Give the extent of all Plasmodium ovale-infected red blood cells.
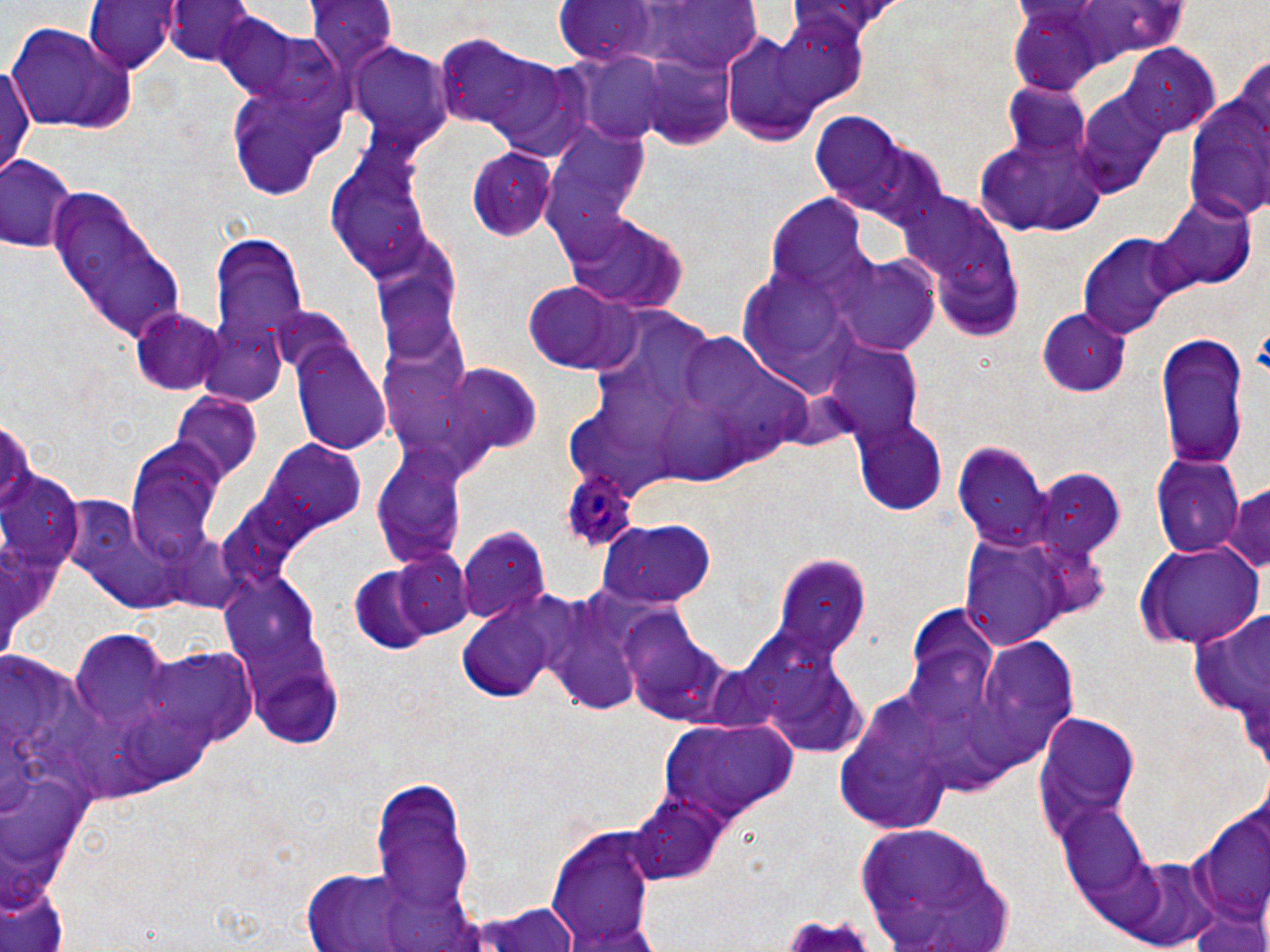
Approximate bounding boxes as [x1, y1, x2, y2] in pixels.
Plasmodium ovale-infected red blood cells: [563, 469, 640, 549].

Uninfected red blood cell locations: [84, 0, 180, 73], [166, 1, 257, 70], [304, 1, 400, 76], [771, 13, 869, 110], [213, 14, 337, 112], [3, 22, 136, 134], [716, 30, 836, 146], [432, 37, 552, 136], [346, 43, 453, 149], [1122, 48, 1218, 136], [572, 53, 677, 147], [640, 56, 741, 149], [486, 57, 597, 159], [0, 59, 36, 181], [221, 73, 348, 203], [1003, 84, 1093, 157], [1074, 89, 1169, 197], [1185, 95, 1269, 225], [807, 109, 943, 225], [971, 123, 1105, 238], [544, 131, 651, 243], [328, 139, 435, 281], [467, 146, 559, 240], [0, 154, 79, 256], [47, 183, 189, 343], [897, 193, 1020, 327], [769, 197, 868, 292], [1151, 199, 1254, 296], [563, 214, 687, 312], [207, 232, 308, 363], [371, 232, 469, 359], [1079, 235, 1186, 336], [834, 255, 940, 354], [522, 279, 636, 374], [268, 306, 356, 382], [131, 307, 225, 394], [1038, 308, 1132, 396], [196, 324, 289, 408], [683, 330, 774, 417], [1153, 334, 1251, 467], [290, 341, 392, 453], [829, 346, 925, 441], [419, 362, 543, 462], [581, 375, 692, 450], [170, 394, 263, 484], [663, 401, 741, 487], [852, 417, 948, 516], [120, 433, 230, 566], [955, 442, 1056, 550], [267, 443, 367, 532], [370, 444, 468, 564], [1153, 455, 1245, 557], [1032, 472, 1126, 561], [1223, 484, 1270, 579], [593, 519, 718, 605], [456, 526, 550, 625], [953, 528, 1096, 650], [1139, 545, 1265, 646], [392, 550, 475, 640], [770, 554, 872, 663], [350, 568, 435, 656], [222, 573, 326, 678], [541, 587, 667, 715], [452, 589, 578, 703], [1184, 600, 1270, 741], [901, 603, 998, 717], [618, 610, 745, 729], [68, 627, 182, 722], [973, 636, 1081, 761], [135, 646, 258, 749], [832, 691, 961, 833], [1030, 709, 1141, 848], [653, 715, 798, 825], [368, 774, 477, 912], [628, 795, 726, 886], [1196, 803, 1270, 930], [1058, 805, 1152, 900], [541, 820, 661, 952], [857, 821, 1012, 951], [1117, 856, 1221, 950], [294, 864, 482, 952], [0, 884, 67, 952], [460, 899, 583, 952], [1186, 904, 1269, 952]. Slide-level diagnosis: Plasmodium ovale. One field of a larger specimen. Thin blood film. Captured at 1000x magnification. Optical microscopy. Image is 1270×952 pixels. May-Grünwald-Giemsa stain.